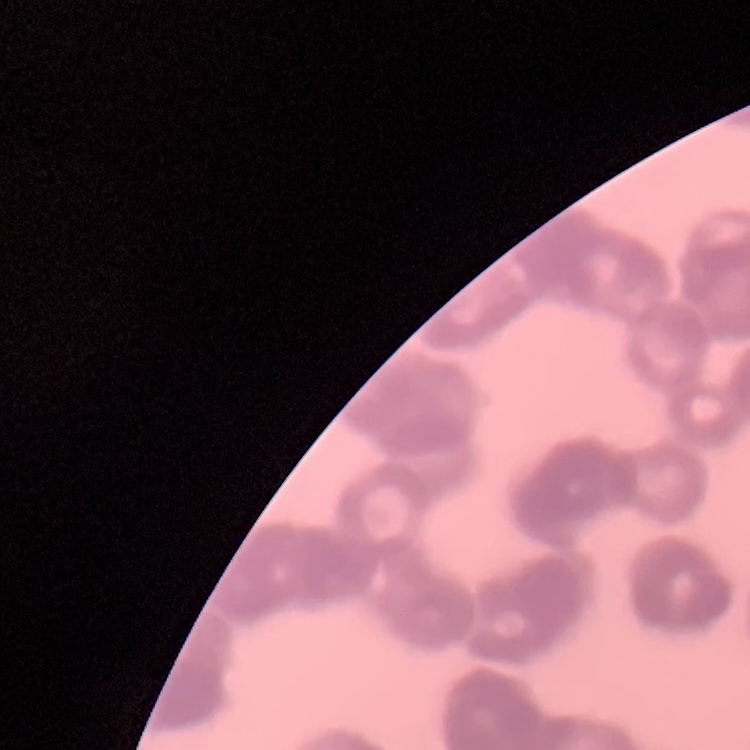
Summary:
  - Red blood cell morphology: rouleaux formation
  - Preparation: thin blood film
  - Stain: Field's or Giemsa
  - Image type: square crop of a larger photomicrograph